Point out each Plasmodium parasite.
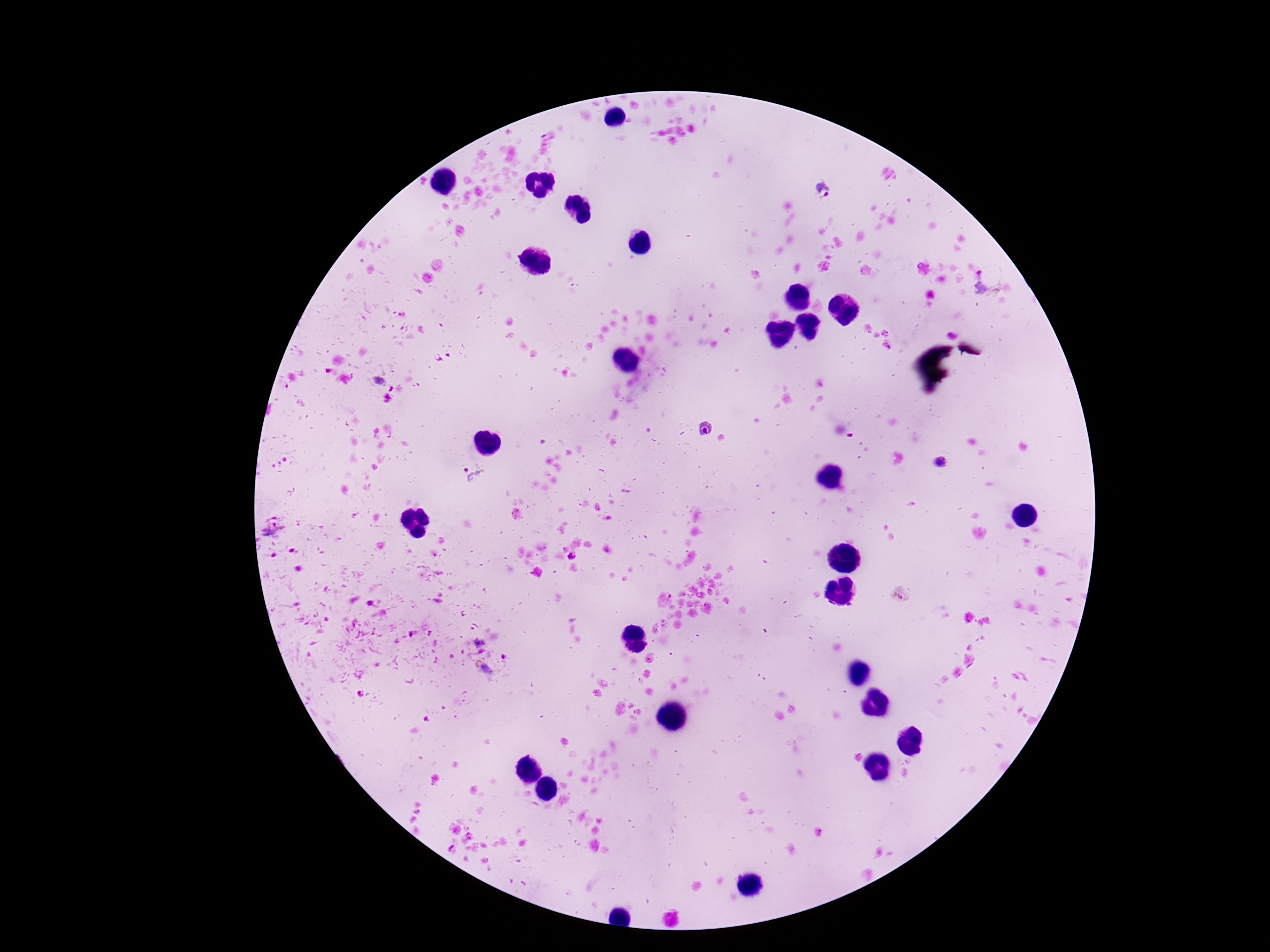
Approximate object centers, in pixels from the top-left corner.
Plasmodium parasites: (x=822, y=191), (x=987, y=285), (x=707, y=428), (x=471, y=475), (x=272, y=529).

Patient malaria status: positive. Smartphone photograph taken through the microscope eyepiece. Single field of view. Thick blood film. 100x magnification. Giemsa-stained preparation. Image is 1270×952 pixels.